Locate every blood parasite and identify its species.
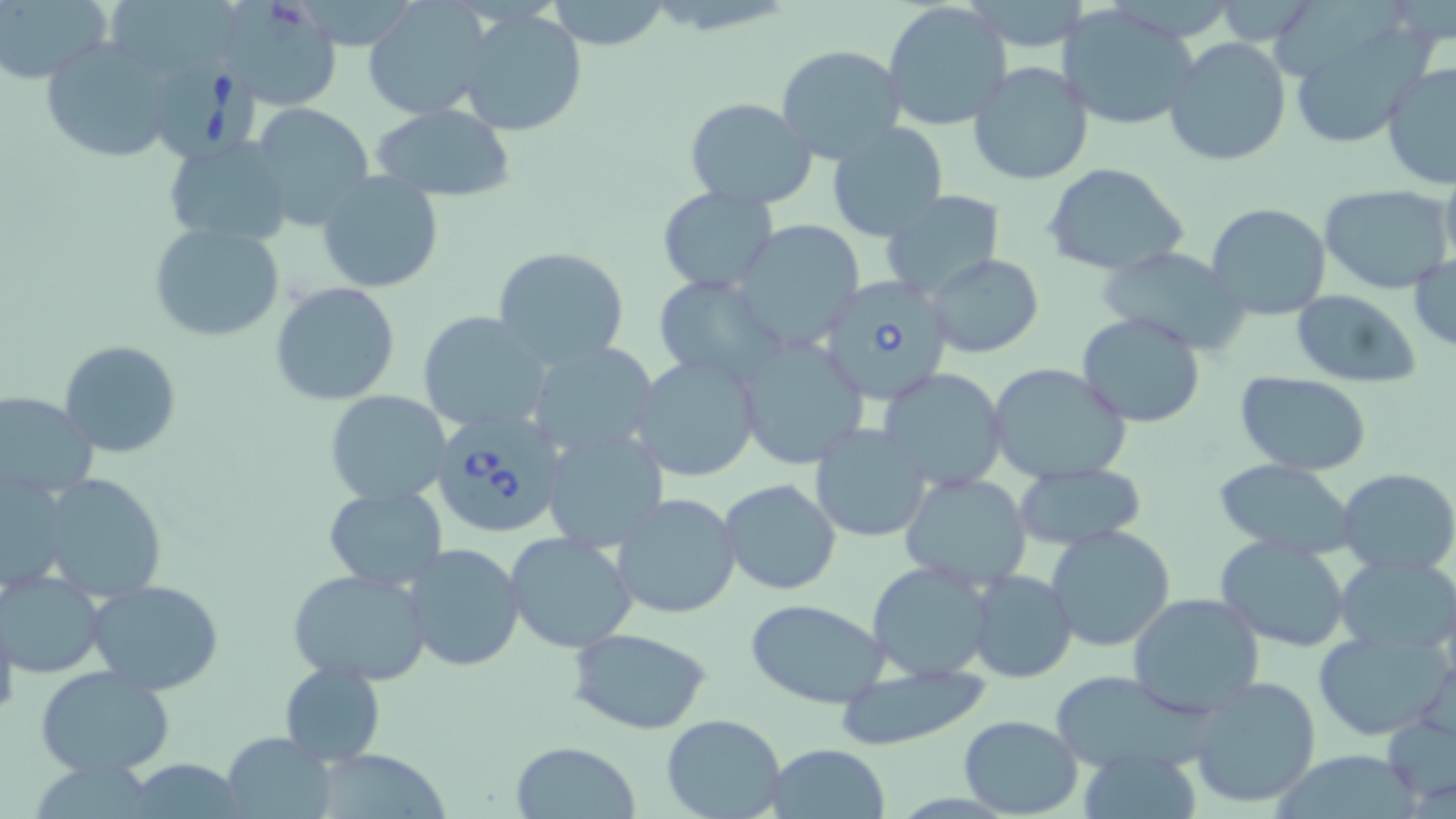
Approximate bounding boxes as named x1/y1/x2/y2 corners in pixels.
Babesia divergens-infected red blood cells: (x1=148, y1=49, x2=265, y2=162), (x1=818, y1=275, x2=953, y2=406), (x1=430, y1=410, x2=567, y2=540).
No Plasmodium falciparum, Plasmodium ovale, Plasmodium malariae, Plasmodium vivax, or Trypanosoma brucei observed.

Uninfected red blood cell locations: (x1=363, y1=0, x2=488, y2=120), (x1=546, y1=0, x2=672, y2=50), (x1=0, y1=1, x2=110, y2=81), (x1=223, y1=1, x2=343, y2=109), (x1=882, y1=1, x2=1013, y2=131), (x1=107, y1=3, x2=247, y2=72), (x1=1055, y1=4, x2=1199, y2=131), (x1=457, y1=8, x2=589, y2=137), (x1=1286, y1=19, x2=1438, y2=150), (x1=42, y1=37, x2=175, y2=165), (x1=1164, y1=37, x2=1293, y2=169), (x1=776, y1=44, x2=906, y2=163), (x1=968, y1=61, x2=1094, y2=186), (x1=1381, y1=62, x2=1456, y2=191), (x1=683, y1=98, x2=818, y2=208), (x1=251, y1=101, x2=373, y2=230), (x1=370, y1=104, x2=520, y2=200), (x1=824, y1=121, x2=950, y2=242), (x1=163, y1=137, x2=294, y2=245), (x1=1041, y1=162, x2=1190, y2=278), (x1=318, y1=171, x2=444, y2=293), (x1=1319, y1=184, x2=1455, y2=296), (x1=658, y1=187, x2=779, y2=293), (x1=881, y1=191, x2=1006, y2=299), (x1=1205, y1=202, x2=1331, y2=320), (x1=730, y1=220, x2=865, y2=351), (x1=149, y1=223, x2=286, y2=343), (x1=493, y1=245, x2=630, y2=370), (x1=1095, y1=245, x2=1250, y2=354), (x1=925, y1=253, x2=1042, y2=358), (x1=1409, y1=254, x2=1456, y2=351), (x1=652, y1=275, x2=783, y2=385), (x1=270, y1=281, x2=401, y2=405), (x1=1290, y1=289, x2=1421, y2=387), (x1=417, y1=311, x2=552, y2=433), (x1=1076, y1=313, x2=1206, y2=427), (x1=735, y1=334, x2=870, y2=468), (x1=59, y1=340, x2=182, y2=457), (x1=526, y1=340, x2=663, y2=458), (x1=631, y1=354, x2=763, y2=482), (x1=986, y1=362, x2=1133, y2=485), (x1=878, y1=367, x2=1009, y2=493), (x1=1235, y1=372, x2=1373, y2=474), (x1=324, y1=389, x2=452, y2=506), (x1=0, y1=391, x2=98, y2=500), (x1=809, y1=423, x2=931, y2=542), (x1=542, y1=428, x2=669, y2=555), (x1=1211, y1=458, x2=1358, y2=558), (x1=1012, y1=462, x2=1146, y2=552), (x1=1, y1=468, x2=69, y2=596), (x1=1338, y1=468, x2=1456, y2=577), (x1=899, y1=471, x2=1034, y2=593), (x1=37, y1=472, x2=169, y2=602), (x1=720, y1=477, x2=842, y2=596), (x1=322, y1=486, x2=447, y2=591), (x1=611, y1=492, x2=741, y2=620), (x1=1045, y1=524, x2=1177, y2=652), (x1=505, y1=531, x2=638, y2=654), (x1=1215, y1=535, x2=1352, y2=653), (x1=405, y1=542, x2=526, y2=670), (x1=1334, y1=553, x2=1456, y2=659), (x1=867, y1=560, x2=997, y2=682), (x1=285, y1=566, x2=433, y2=684), (x1=969, y1=568, x2=1077, y2=684), (x1=1, y1=570, x2=104, y2=677), (x1=86, y1=579, x2=225, y2=696), (x1=1127, y1=592, x2=1266, y2=717), (x1=746, y1=599, x2=892, y2=708), (x1=0, y1=603, x2=19, y2=726), (x1=569, y1=627, x2=712, y2=734), (x1=1312, y1=628, x2=1452, y2=741), (x1=279, y1=661, x2=385, y2=766), (x1=836, y1=664, x2=991, y2=751), (x1=36, y1=667, x2=175, y2=779), (x1=1048, y1=670, x2=1219, y2=772), (x1=1188, y1=675, x2=1323, y2=810), (x1=660, y1=713, x2=786, y2=819), (x1=1382, y1=713, x2=1456, y2=810), (x1=958, y1=714, x2=1084, y2=817), (x1=221, y1=732, x2=337, y2=819), (x1=510, y1=740, x2=642, y2=818), (x1=766, y1=742, x2=892, y2=818), (x1=329, y1=747, x2=453, y2=819). Slide-level diagnosis: Babesia divergens. Single field of view. Thin blood smear. May-Grünwald-Giemsa-stained preparation. Image is 1456×819 pixels. 1000x magnification. Light microscopy.